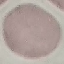

Result: negative for malaria parasites. Giemsa stain. Acquired by smartphone through the microscope eyepiece. Cell patch, automatically extracted from a larger field of view and resized to 64 × 64 pixels. Thin blood smear.